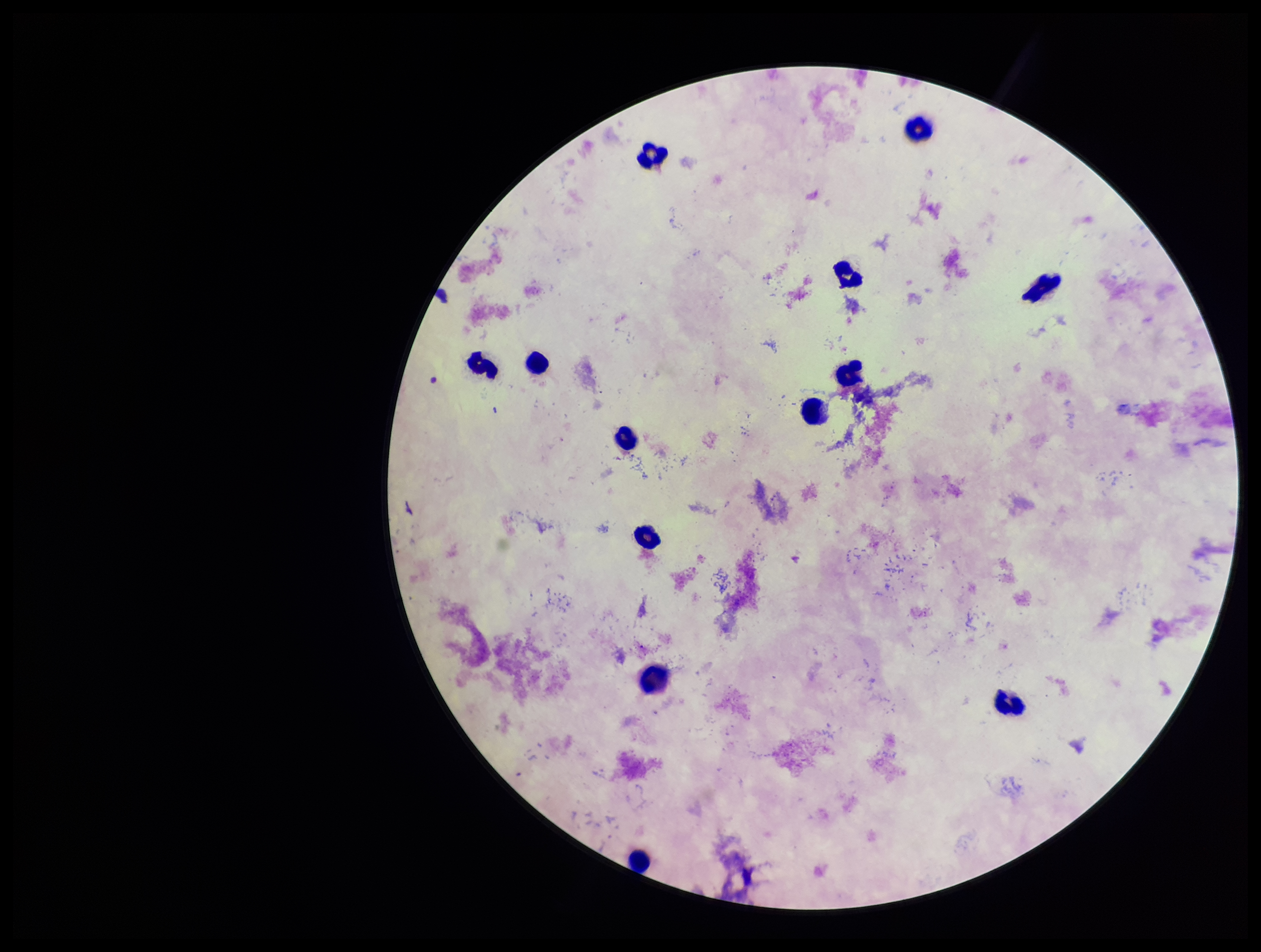

{
  "species_reported_for_this_patient": "Plasmodium falciparum",
  "capture": "smartphone photograph through the microscope eyepiece",
  "plasmodium_parasites": "none identified",
  "image_size": "1261×952 pixels",
  "patient_malaria_status": "positive",
  "preparation": "thick",
  "field_of_view": "one from this slide",
  "stain": "Giemsa",
  "parasite_count": 0,
  "leukocyte_count": 13
}